Assess the morphology of the red blood cells.
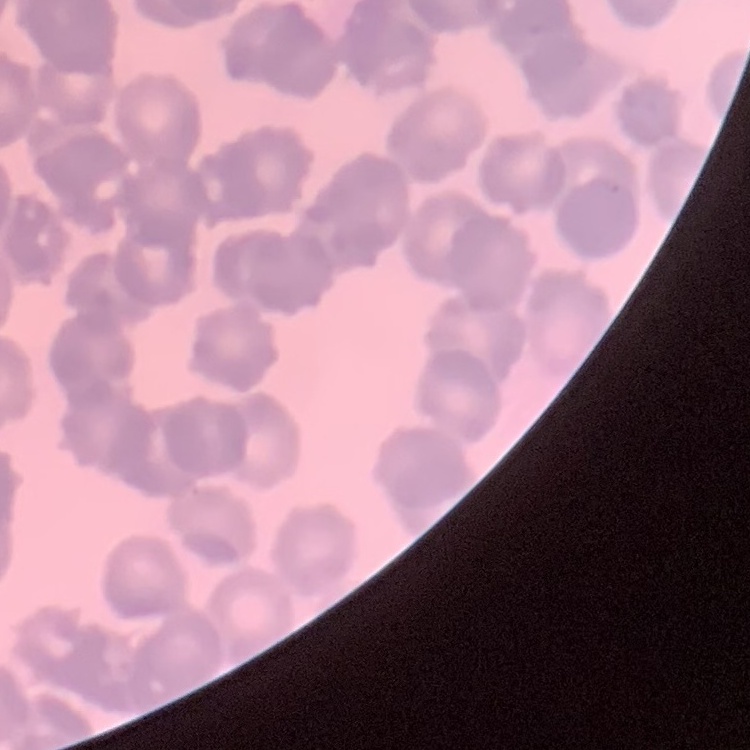

They show rouleaux formation.

Thin peripheral smear. One tile cut from a larger photomicrograph. Field's or Giemsa stain.